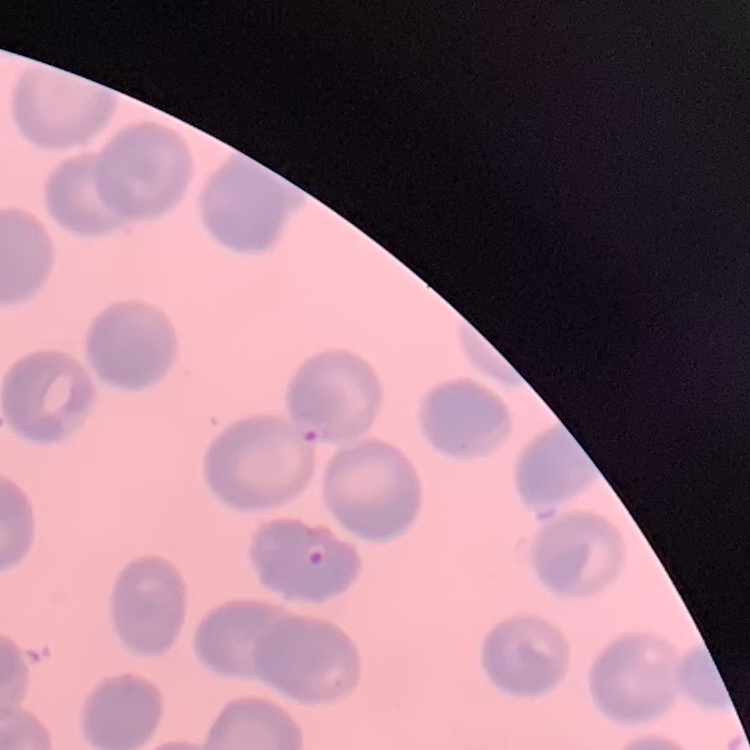
The erythrocytes exhibit no rouleaux formation. Thin blood film. Stained with either Field's or Giemsa. Square crop of a larger photomicrograph.